State which malaria species this is.
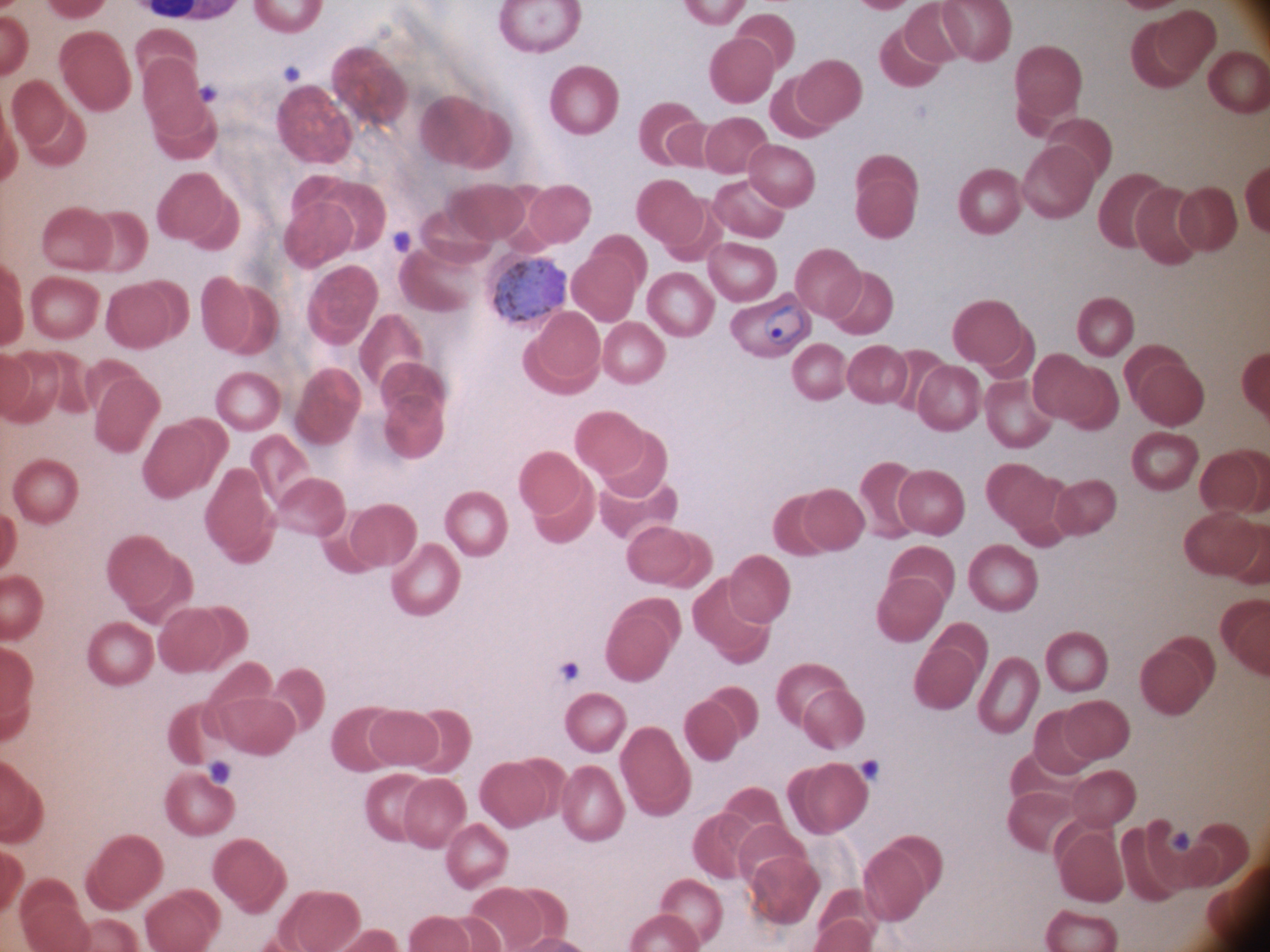

Plasmodium ovale.

life-cycle stages among the annotated parasites = ring form, gametocyte
field of view = one from this slide
magnification = 100x
image size = 1270×952 pixels
stain = Giemsa
microscope = Leica DM2000 with built-in camera
malaria parasite locations = approximate bounding boxes as [x1, y1, x2, y2] in pixels, from the source annotation, which is not necessarily exhaustive: [493, 257, 567, 324], [762, 304, 812, 346]
preparation = thin blood film